Assess this cell for malaria.
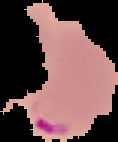
Parasitized.

{
  "image_type": "segmented cell region with the area outside set to black",
  "preparation": "thin blood smear",
  "image_size": "118×142 pixels"
}